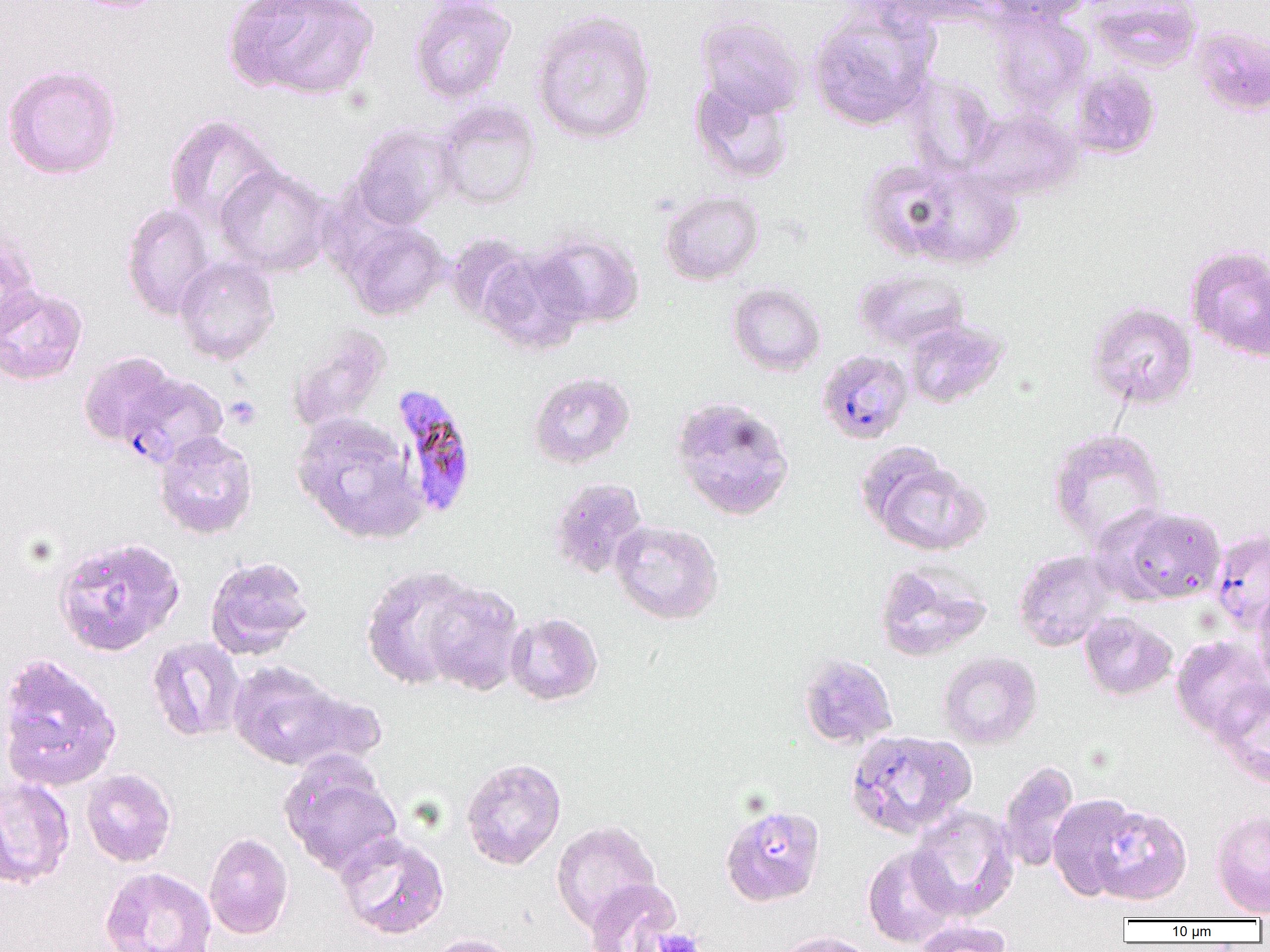
Approximate bounding boxes as named x1/y1/x2/y2 corners in pixels. Platelet locations: (x1=224, y1=395, x2=262, y2=430), (x1=650, y1=927, x2=703, y2=952). Plasmodium falciparum-infected red blood cell locations: (x1=817, y1=349, x2=914, y2=445), (x1=118, y1=371, x2=229, y2=469), (x1=391, y1=383, x2=478, y2=519), (x1=1209, y1=529, x2=1270, y2=635). Uninfected red blood cell locations: (x1=64, y1=0, x2=174, y2=13), (x1=409, y1=0, x2=517, y2=104), (x1=886, y1=0, x2=994, y2=26), (x1=984, y1=0, x2=1092, y2=26), (x1=1089, y1=0, x2=1202, y2=73), (x1=223, y1=1, x2=380, y2=101), (x1=808, y1=5, x2=938, y2=132), (x1=531, y1=9, x2=657, y2=145), (x1=991, y1=9, x2=1092, y2=113), (x1=695, y1=14, x2=806, y2=119), (x1=1190, y1=24, x2=1270, y2=116), (x1=1, y1=63, x2=123, y2=180), (x1=1070, y1=66, x2=1161, y2=160), (x1=903, y1=73, x2=999, y2=176), (x1=689, y1=79, x2=795, y2=185), (x1=433, y1=100, x2=541, y2=209), (x1=967, y1=108, x2=1083, y2=200), (x1=163, y1=115, x2=281, y2=229), (x1=350, y1=122, x2=459, y2=230), (x1=859, y1=158, x2=961, y2=261), (x1=214, y1=164, x2=333, y2=277), (x1=904, y1=165, x2=1024, y2=270), (x1=659, y1=190, x2=764, y2=285), (x1=120, y1=203, x2=217, y2=321), (x1=343, y1=219, x2=449, y2=321), (x1=0, y1=229, x2=42, y2=342), (x1=530, y1=229, x2=644, y2=329), (x1=444, y1=233, x2=536, y2=325), (x1=1185, y1=245, x2=1270, y2=363), (x1=477, y1=249, x2=588, y2=356), (x1=174, y1=256, x2=280, y2=365), (x1=854, y1=268, x2=971, y2=352), (x1=727, y1=282, x2=826, y2=377), (x1=0, y1=284, x2=88, y2=386), (x1=1086, y1=301, x2=1198, y2=410), (x1=903, y1=319, x2=1008, y2=409), (x1=286, y1=326, x2=391, y2=434), (x1=78, y1=350, x2=183, y2=453), (x1=527, y1=371, x2=635, y2=469), (x1=669, y1=395, x2=796, y2=521), (x1=291, y1=412, x2=426, y2=544), (x1=1048, y1=427, x2=1168, y2=549), (x1=153, y1=431, x2=258, y2=539), (x1=862, y1=450, x2=989, y2=556), (x1=548, y1=477, x2=649, y2=579), (x1=1105, y1=505, x2=1226, y2=605), (x1=610, y1=520, x2=723, y2=625), (x1=53, y1=536, x2=185, y2=657), (x1=1013, y1=549, x2=1119, y2=651), (x1=205, y1=555, x2=314, y2=659), (x1=873, y1=561, x2=992, y2=662), (x1=361, y1=565, x2=479, y2=690), (x1=421, y1=582, x2=526, y2=696), (x1=1252, y1=587, x2=1270, y2=693), (x1=1079, y1=611, x2=1177, y2=701), (x1=506, y1=614, x2=605, y2=708), (x1=147, y1=636, x2=245, y2=742), (x1=1171, y1=636, x2=1270, y2=741), (x1=937, y1=651, x2=1042, y2=749), (x1=0, y1=653, x2=122, y2=793), (x1=797, y1=653, x2=898, y2=749), (x1=228, y1=661, x2=349, y2=770), (x1=1213, y1=685, x2=1270, y2=789), (x1=279, y1=688, x2=389, y2=772), (x1=845, y1=729, x2=975, y2=839), (x1=278, y1=753, x2=402, y2=878), (x1=461, y1=757, x2=566, y2=870), (x1=998, y1=760, x2=1080, y2=873), (x1=81, y1=769, x2=176, y2=867), (x1=0, y1=776, x2=75, y2=889), (x1=1048, y1=793, x2=1142, y2=901), (x1=1088, y1=802, x2=1192, y2=905), (x1=720, y1=804, x2=826, y2=907), (x1=907, y1=805, x2=1019, y2=922), (x1=1210, y1=808, x2=1270, y2=917), (x1=551, y1=820, x2=662, y2=933), (x1=204, y1=831, x2=294, y2=940), (x1=336, y1=832, x2=450, y2=939), (x1=862, y1=845, x2=958, y2=948), (x1=99, y1=867, x2=217, y2=952), (x1=584, y1=879, x2=684, y2=952), (x1=913, y1=920, x2=1013, y2=952), (x1=774, y1=930, x2=878, y2=952), (x1=425, y1=933, x2=523, y2=952). Slide-level diagnosis: Plasmodium falciparum. 1000x magnification. Image is 1270×952 pixels. Thin blood film. One field of a larger specimen. Optical microscopy.